Name the parasite shown.
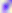
This is Toxoplasma gondii.

magnification: 400x
modality: photomicrograph